Name the parasite shown.
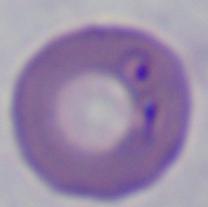
This is Babesia.

magnification: 1000x
modality: photomicrograph